Outline every leukocyte.
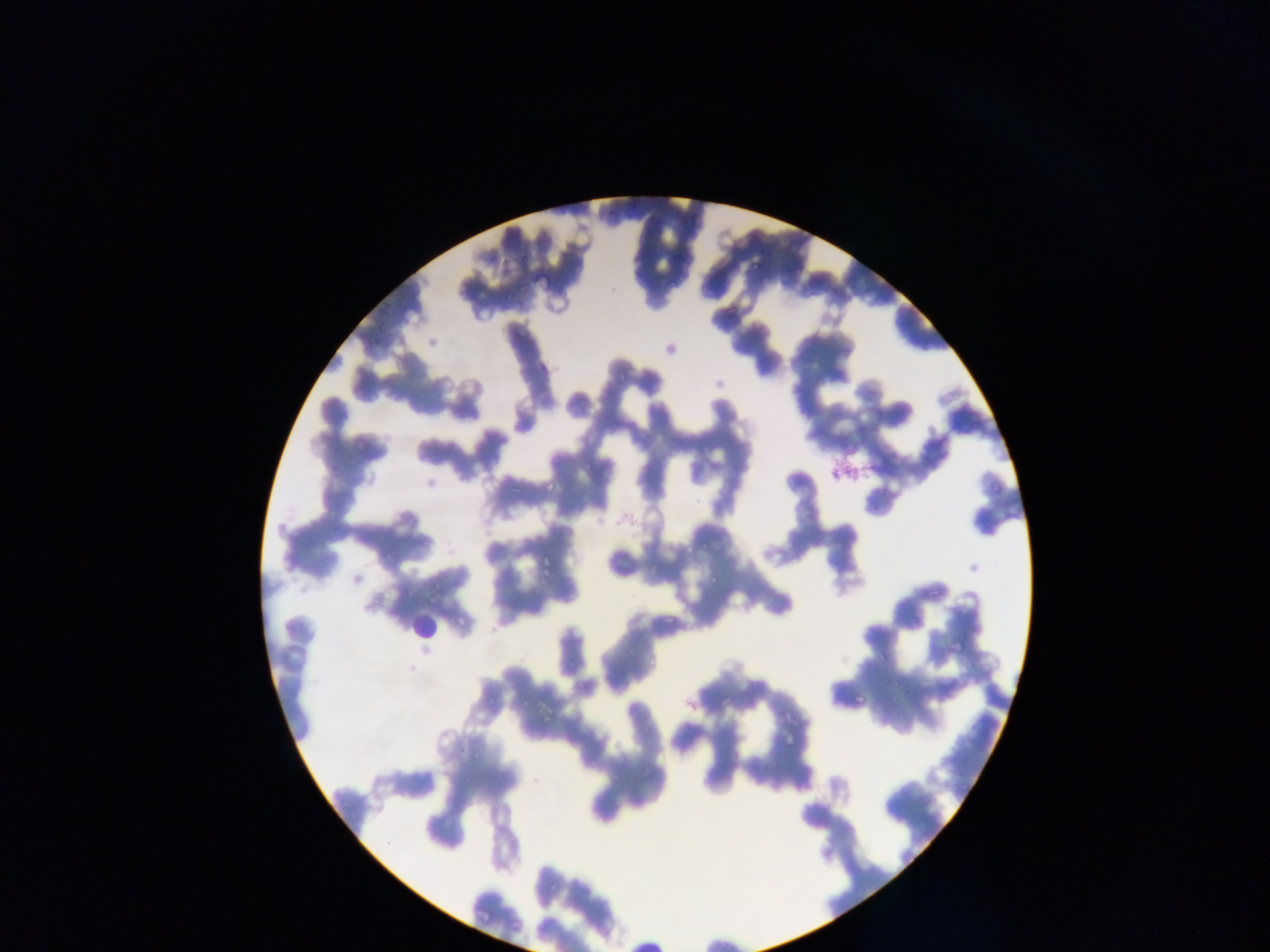

Approximate bounding boxes as {left, top, right, bottom} in pixels.
Leukocytes: {408, 598, 452, 643}.

Malaria parasite locations: {617, 370, 631, 384}, {868, 416, 884, 437}, {581, 459, 594, 469}, {544, 478, 556, 491}, {988, 480, 1000, 494}, {702, 542, 714, 554}, {540, 555, 555, 573}, {697, 562, 727, 588}, {663, 606, 683, 625}, {950, 637, 969, 658}, {854, 693, 868, 705}. Mobile-phone photograph taken through the microscope. One field of view. Image is 1270×952 pixels. Thin blood film. Collected in Ghana.